Classify this cell by malaria status.
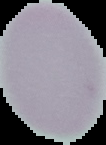

It is uninfected.

Summary:
  - Image type: segmented cell region on a black background
  - Image size: 106×145 pixels
  - Preparation: thin blood smear